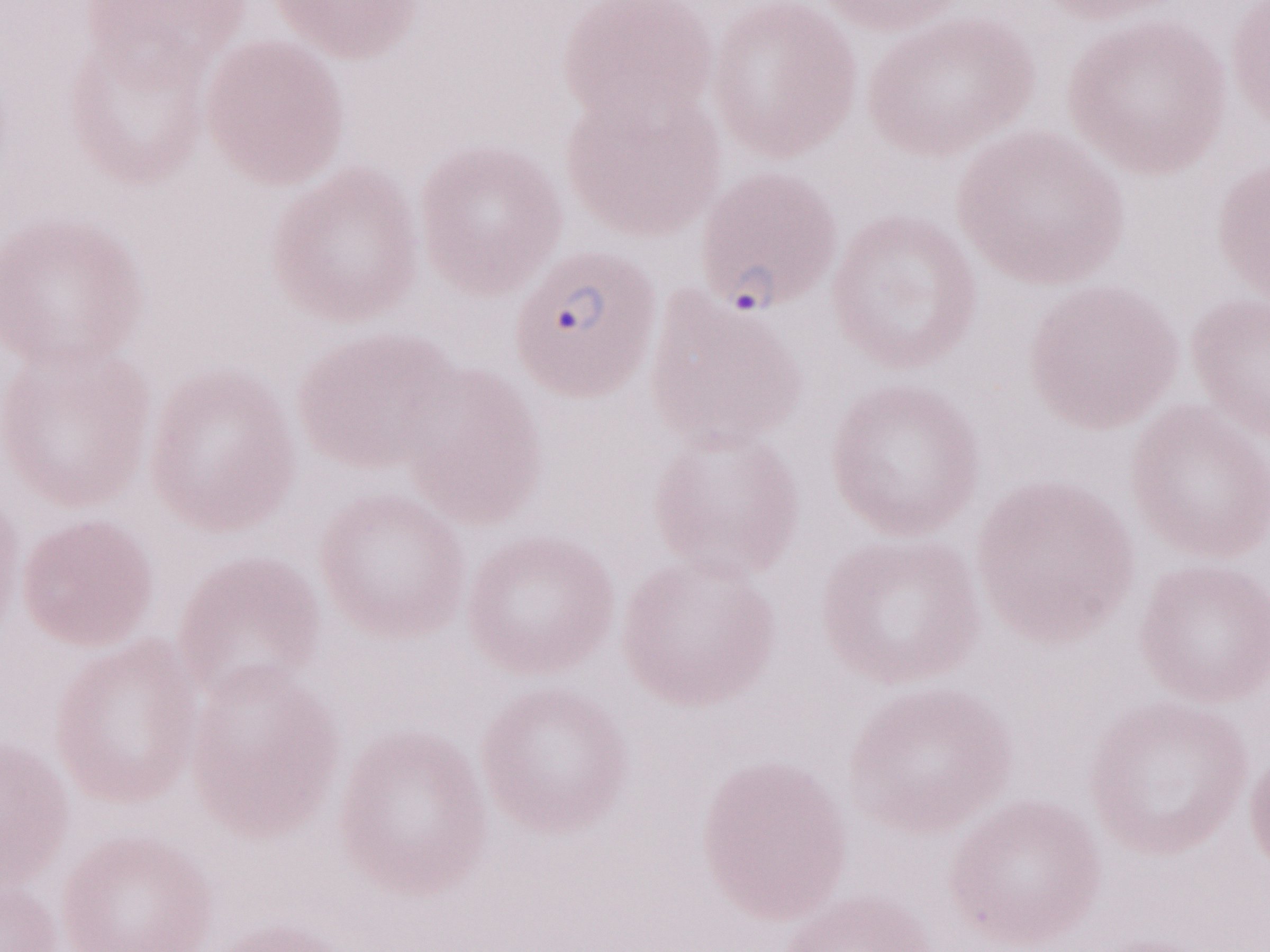
1,000x magnification. Olympus BX43 microscope and DP73 digital camera. Patient-level malaria diagnosis: positive. May-Grünwald-Giemsa (MGG) stain. One field of this slide. Image is 1270×952 pixels. Thin blood film.